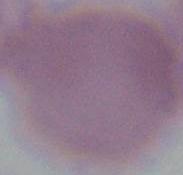

1000x magnification. Photomicrograph. A red blood cell is seen.